Name the cell type shown.
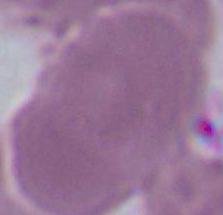
This is an erythrocyte.

modality = photomicrograph
magnification = 1000x